Identify the parasite.
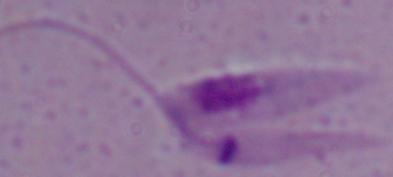
Leishmania.

Summary:
  - Modality: micrograph
  - Magnification: 1000x